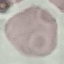
Summary:
  - Malaria status: uninfected
  - Preparation: thin smear
  - Capture: smartphone through the microscope eyepiece
  - Stain: Giemsa
  - Image type: cell patch, automatically extracted from a larger field of view and resized to 64 × 64 pixels